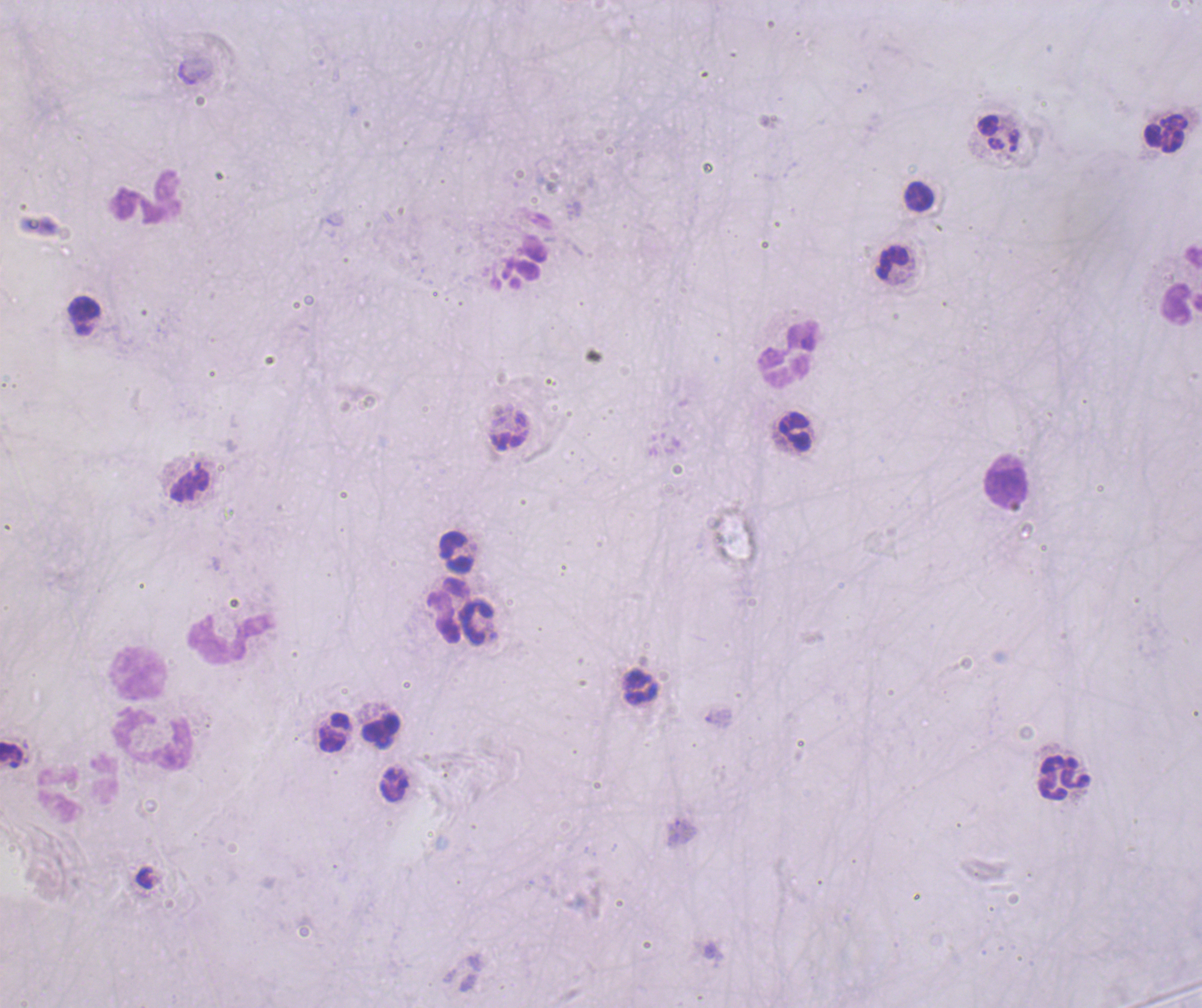
Approximate centers as [x, y] in pixels.
Summary:
  - Leukocyte locations: [1166, 134], [918, 196], [145, 197], [892, 262], [1182, 303], [84, 309], [788, 353], [794, 432], [190, 483], [1006, 487], [455, 552], [446, 610], [476, 622], [230, 638], [138, 672], [640, 686], [382, 727], [334, 731], [152, 740], [1063, 778], [78, 788]
  - Background quality: poor
  - Stain: Romanowsky
  - Result: negative for Plasmodium parasites
  - Preparation: thick smear of blood
  - Magnification: 100x
  - Coloration quality: bad
  - Field of view: single
  - Context: previously used in an actual diagnosis
  - Image size: 1202×1008 pixels